Classify this cell by malaria status.
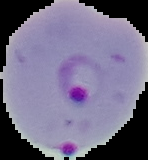
Parasitized.

{
  "image_type": "segmented cell region with the area outside set to black",
  "preparation": "thin blood smear",
  "image_size": "148×160 pixels"
}